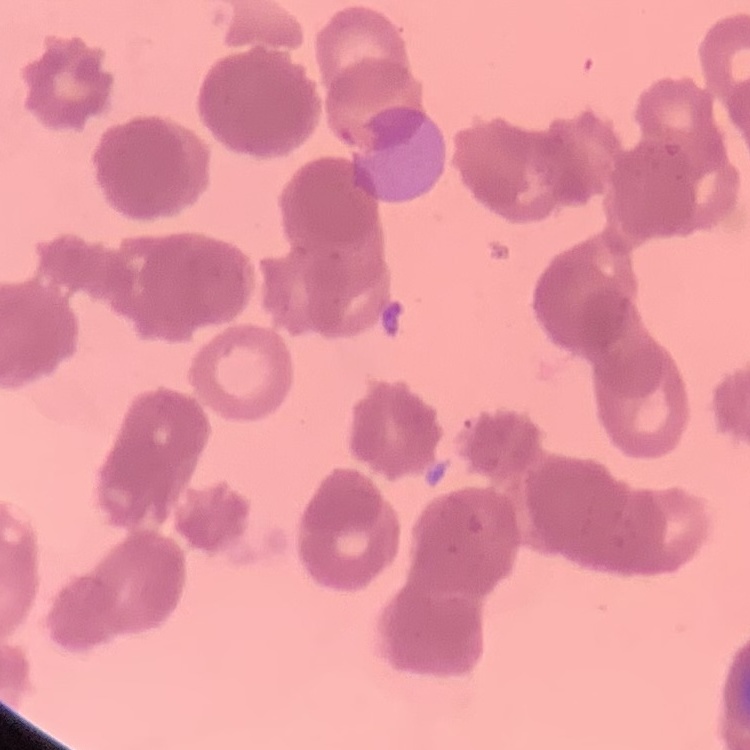

Summary:
  - Red blood cell morphology: rouleaux formation
  - Image type: square crop of a larger photomicrograph
  - Stain: Field's or Giemsa
  - Preparation: thin blood smear